Point out each Plasmodium parasite.
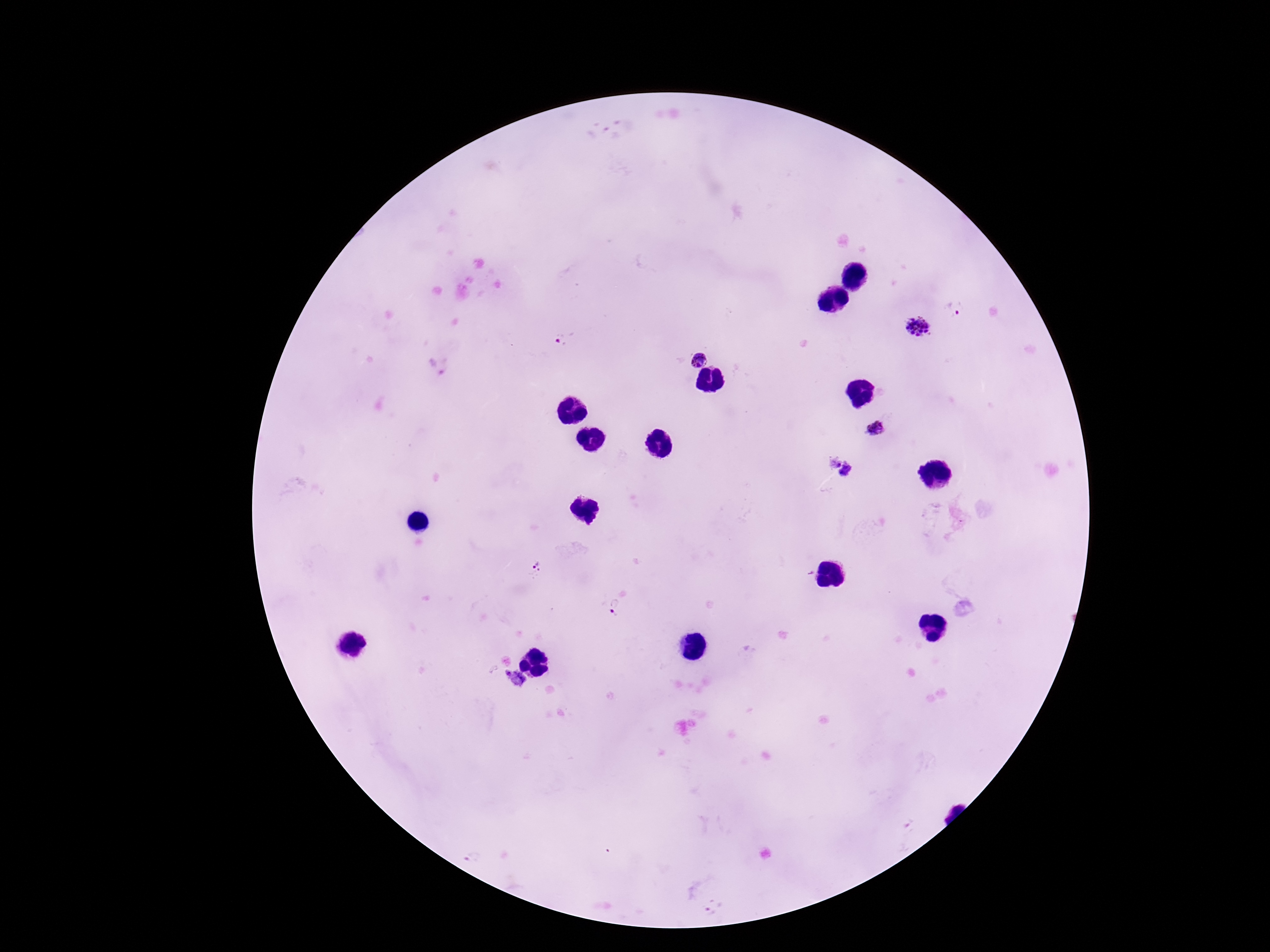

Approximate object centers, in pixels from the top-left corner.
Plasmodium parasites: (x=954, y=310), (x=917, y=328), (x=563, y=340), (x=699, y=360), (x=438, y=365), (x=877, y=428), (x=831, y=461), (x=849, y=473), (x=535, y=566), (x=617, y=607), (x=507, y=672), (x=517, y=678), (x=472, y=857), (x=713, y=907).

field of view = one from this slide
stain = Giemsa
image size = 1270×952 pixels
preparation = thick peripheral-blood smear
capture = smartphone camera through the microscope eyepiece
patient malaria status = infected
magnification = 100x